Locate every blood parasite and identify its species.
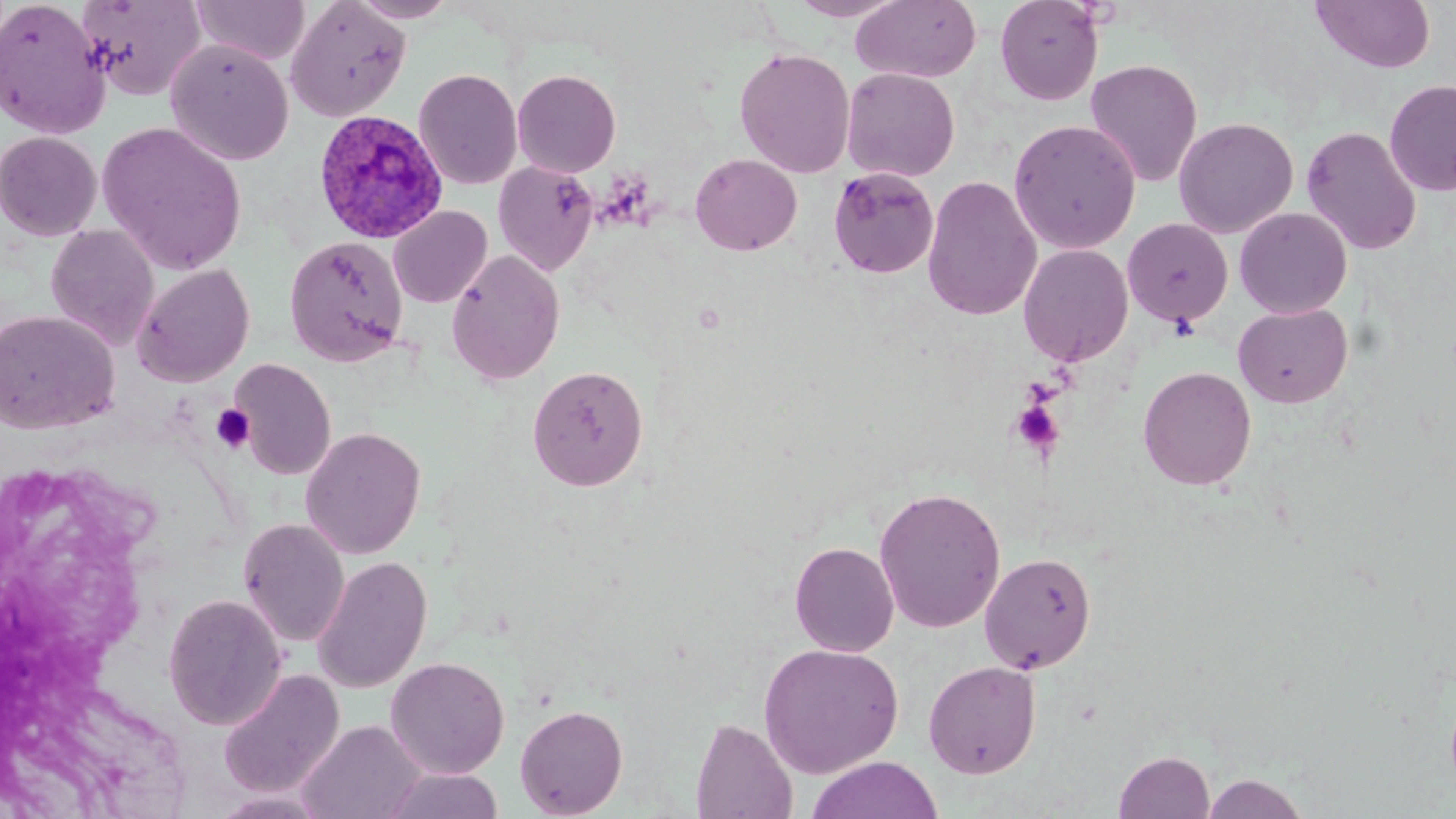
Approximate bounding boxes as (x1,y1)-(x2,y2) corner pairs in pixels.
Plasmodium ovale-infected red blood cells: (313,109)-(449,244).
No Plasmodium falciparum, Plasmodium malariae, Plasmodium vivax, Babesia divergens, or Trypanosoma brucei observed.

Platelet locations: (1009,399)-(1066,459), (212,404)-(255,453). Uninfected red blood cell locations: (0,0)-(111,139), (77,0)-(206,101), (190,0)-(311,65), (349,0)-(459,23), (788,0)-(907,21), (851,0)-(982,83), (994,0)-(1104,106), (1310,0)-(1435,74), (285,1)-(412,121), (165,39)-(294,165), (734,47)-(855,178), (1084,58)-(1203,188), (842,67)-(960,182), (414,68)-(522,189), (512,69)-(621,177), (1384,79)-(1456,196), (1173,117)-(1298,238), (1007,118)-(1142,254), (97,122)-(248,276), (1301,125)-(1422,256), (0,131)-(103,241), (689,153)-(802,256), (494,161)-(599,276), (828,166)-(940,279), (922,174)-(1042,321), (389,206)-(492,308), (1234,207)-(1352,319), (1122,218)-(1234,327), (45,224)-(160,350), (284,235)-(409,366), (1018,243)-(1134,367), (446,249)-(565,386), (133,263)-(255,387), (1233,303)-(1353,408), (0,309)-(120,434), (230,359)-(337,481), (527,364)-(649,492), (1137,366)-(1257,491), (300,426)-(426,559), (873,486)-(1007,633), (238,519)-(350,647), (789,541)-(899,656), (979,551)-(1097,674), (312,556)-(432,693), (163,593)-(287,729), (758,643)-(904,778), (386,657)-(510,778), (923,660)-(1041,779), (217,669)-(345,799), (514,703)-(628,818), (690,716)-(797,818), (298,719)-(427,819), (1113,749)-(1216,819), (806,756)-(944,819), (381,768)-(504,819), (1200,772)-(1311,819), (210,790)-(333,818). Slide-level diagnosis: Plasmodium ovale. Light microscopy. One field of a larger specimen. May-Grünwald-Giemsa stain. Thin blood film. 1000x magnification. Image is 1456×819 pixels.